Locate every Plasmodium malariae-infected red blood cell.
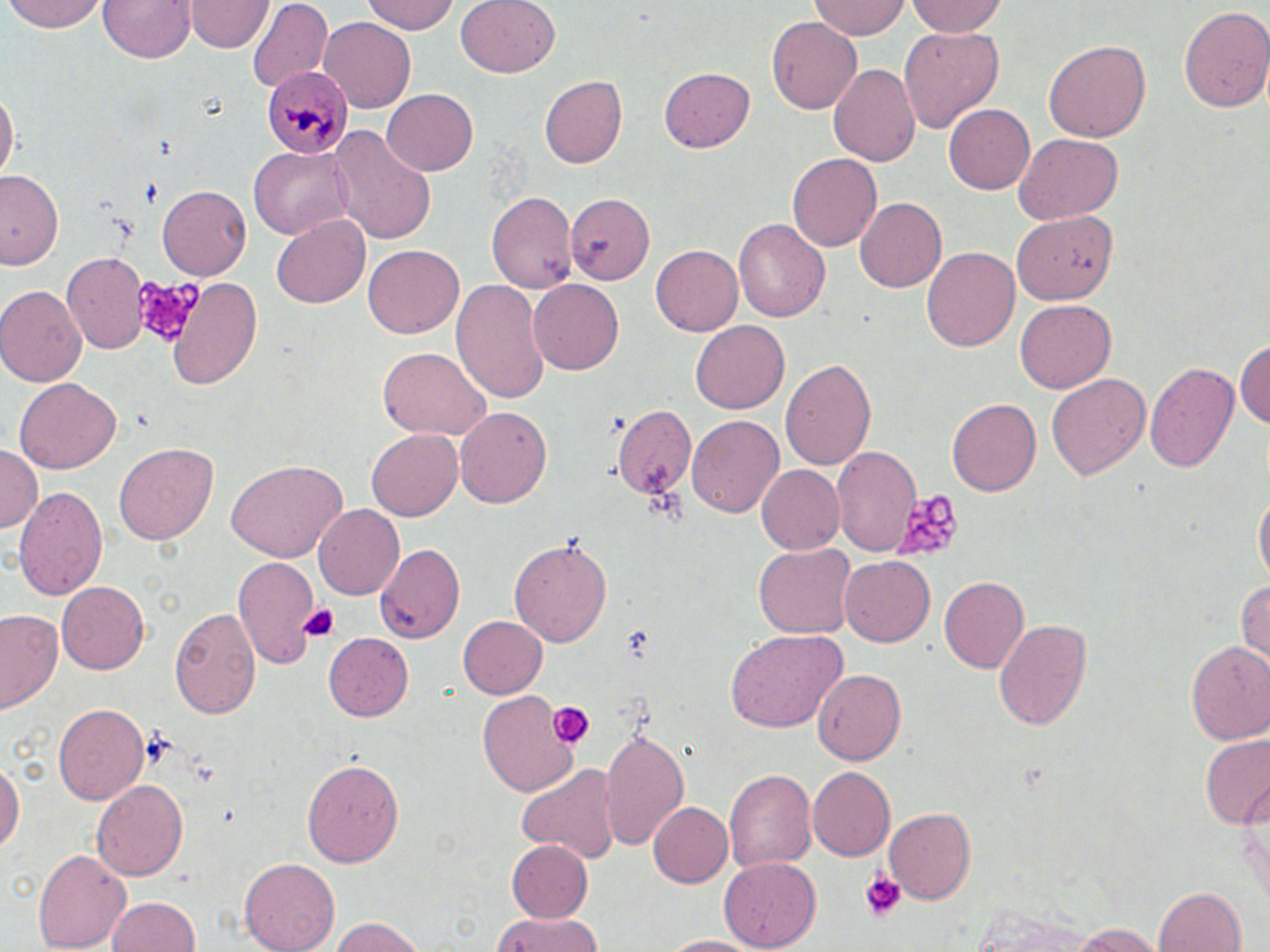

Approximate bounding boxes as (x1, y1, x2, y2) in pixels.
Plasmodium malariae-infected red blood cells: (262, 65, 354, 155).

Summary:
  - Uninfected red blood cell locations: (6, 0, 110, 32), (99, 0, 195, 64), (363, 0, 459, 35), (454, 0, 560, 79), (808, 0, 910, 41), (906, 0, 1010, 38), (187, 1, 271, 53), (247, 1, 332, 91), (1179, 5, 1270, 116), (319, 18, 417, 111), (767, 18, 863, 113), (897, 26, 1005, 133), (1043, 40, 1151, 142), (828, 60, 923, 168), (660, 64, 755, 150), (538, 74, 626, 168), (383, 87, 479, 175), (0, 90, 18, 186), (944, 104, 1036, 196), (330, 126, 438, 246), (1013, 134, 1123, 223), (248, 146, 355, 238), (786, 153, 882, 252), (0, 170, 64, 271), (157, 184, 251, 280), (486, 190, 579, 293), (565, 194, 654, 280), (854, 197, 945, 293), (1016, 211, 1115, 303), (271, 215, 369, 309), (733, 217, 832, 322), (651, 242, 746, 336), (363, 243, 464, 338), (924, 245, 1020, 353), (63, 252, 149, 354), (167, 276, 263, 389), (452, 279, 551, 405), (529, 279, 625, 375), (0, 285, 87, 385), (1016, 300, 1118, 393), (691, 319, 788, 411), (1235, 335, 1270, 435), (377, 348, 488, 441), (780, 358, 877, 469), (1146, 361, 1241, 475), (1046, 372, 1152, 481), (14, 379, 120, 474), (948, 399, 1041, 498), (609, 403, 696, 498), (455, 406, 552, 510), (687, 415, 784, 519), (366, 428, 463, 521), (113, 442, 217, 543), (0, 446, 42, 534), (834, 446, 921, 556), (227, 458, 346, 559), (756, 464, 844, 553), (13, 484, 109, 602), (1254, 487, 1269, 592), (312, 505, 404, 600), (510, 535, 613, 647), (374, 540, 466, 644), (755, 543, 854, 638), (234, 555, 321, 672), (838, 555, 936, 647), (940, 576, 1032, 674), (1235, 578, 1270, 671), (56, 580, 149, 675), (170, 606, 260, 722), (1, 608, 64, 714), (456, 613, 547, 699), (993, 616, 1092, 733), (726, 629, 843, 735), (325, 633, 415, 720), (1185, 638, 1270, 744), (813, 668, 907, 765), (475, 690, 581, 799), (54, 702, 146, 804), (600, 727, 690, 852), (1200, 734, 1270, 829), (0, 754, 23, 858), (300, 756, 404, 868), (516, 760, 624, 864), (806, 767, 895, 862), (723, 769, 815, 872), (91, 778, 188, 881), (648, 801, 731, 886), (883, 807, 975, 905), (505, 840, 592, 923), (33, 845, 130, 952), (239, 857, 340, 952), (719, 858, 818, 950), (1153, 887, 1245, 952), (106, 895, 202, 952), (960, 903, 1106, 952), (488, 914, 608, 952), (327, 916, 429, 952), (1070, 924, 1165, 951), (652, 932, 768, 950)
  - Platelet locations: (136, 178, 166, 204), (108, 214, 140, 243), (132, 274, 199, 347), (889, 490, 962, 557), (301, 602, 341, 642), (617, 624, 657, 664), (547, 701, 593, 749), (860, 871, 907, 921)
  - Slide-level diagnosis: Plasmodium malariae
  - Image size: 1270×952 pixels
  - Modality: optical microscopy
  - Stain: May-Grünwald-Giemsa
  - Magnification: 1000x
  - Preparation: thin blood film
  - Field of view: single